Evaluate for Plasmodium parasites.
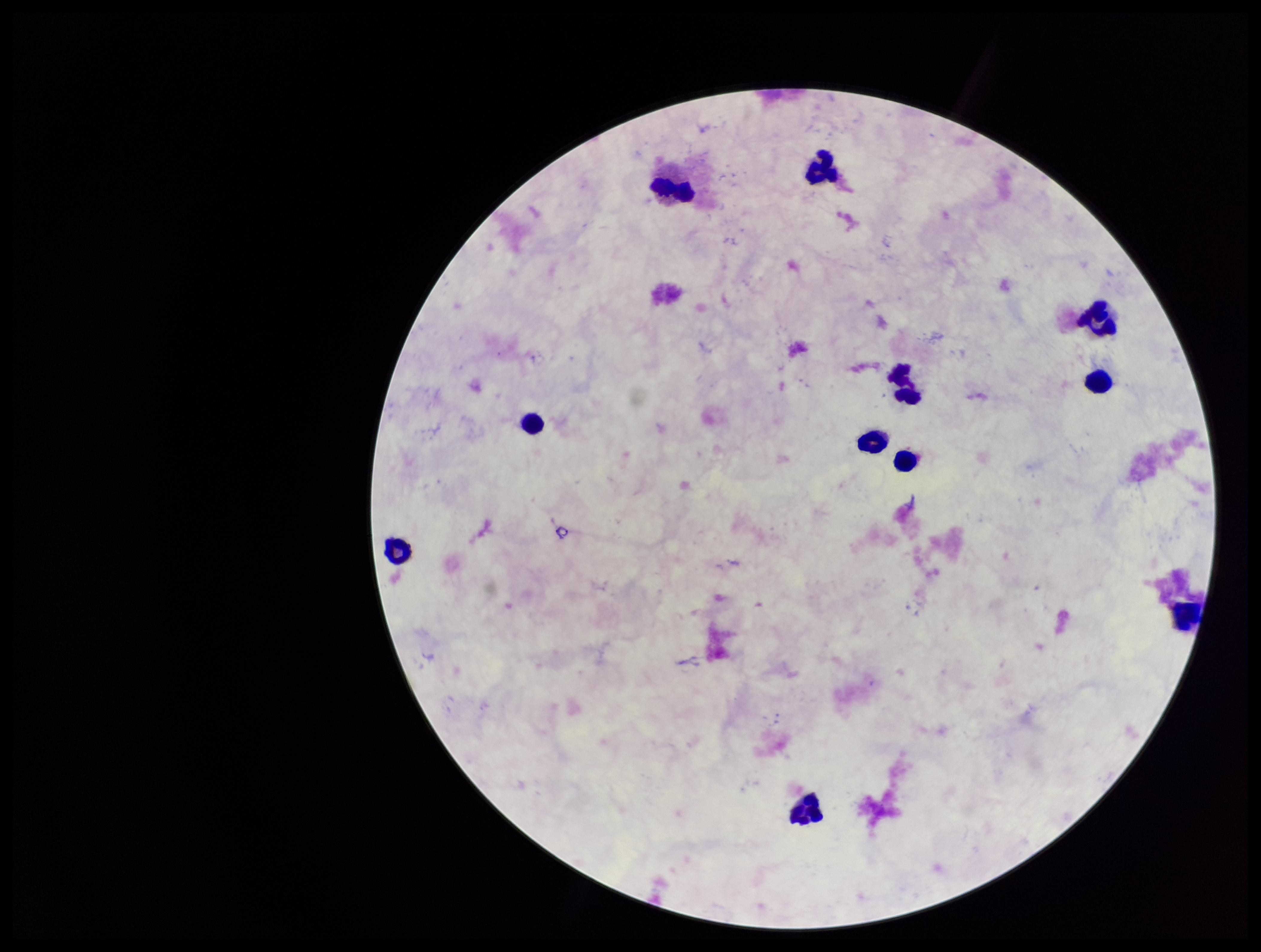

None identified.

Summary:
  - Parasite count: 0
  - Image size: 1261×952 pixels
  - Stain: Giemsa
  - Leukocyte count: 11
  - Capture: smartphone photograph through the microscope eyepiece
  - Field of view: one from this slide
  - Preparation: thick
  - Patient malaria status: negative